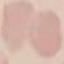

result: no malaria parasites seen
stain: Giemsa
image_type: cell patch, automatically extracted from a larger field of view and resized to 64 × 64 pixels
capture: smartphone camera at the microscope eyepiece
preparation: thin blood smear